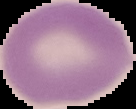

image_type: segmented cell region with the area outside set to black
preparation: thin blood smear
image_size: 136×109 pixels
malaria_status: uninfected